Identify the preparation type.
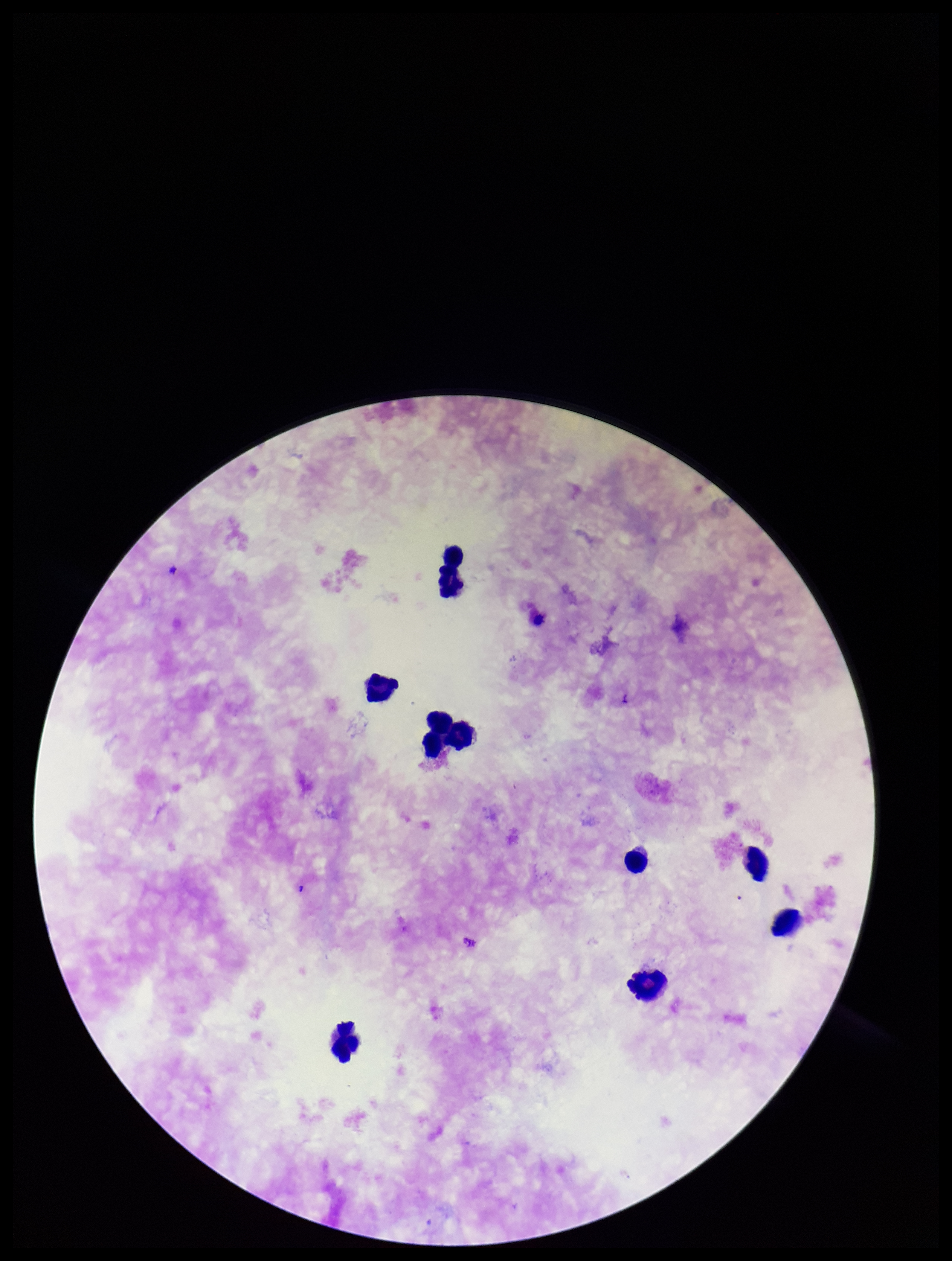
A thick smear.

{
  "capture": "smartphone photograph through the microscope eyepiece",
  "image_size": "952×1261 pixels",
  "species_reported_for_this_patient": "Plasmodium falciparum",
  "field_of_view": "single",
  "patient_malaria_status": "infected",
  "parasite_count": 0,
  "leukocyte_count": 10,
  "plasmodium_parasites": "none detected",
  "stain": "Giemsa"
}